Assess this cell for malaria.
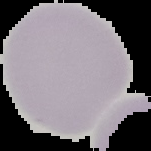

It is uninfected.

Summary:
  - Image type: cell region segmented out of the field of view; surrounding area masked to black
  - Preparation: thin blood smear
  - Image size: 151×151 pixels